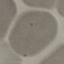 Malaria status: uninfected. Photographed with a smartphone camera at the microscope eyepiece. Cell patch, automatically extracted from a larger field of view and resized to 64 × 64 pixels. Thin blood smear. Giemsa-stained preparation.